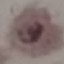
Result: malaria parasites detected. Giemsa stain. Thin blood film. Automatically extracted cell patch, resized to 64 × 64 pixels. Acquired by smartphone through the microscope eyepiece.